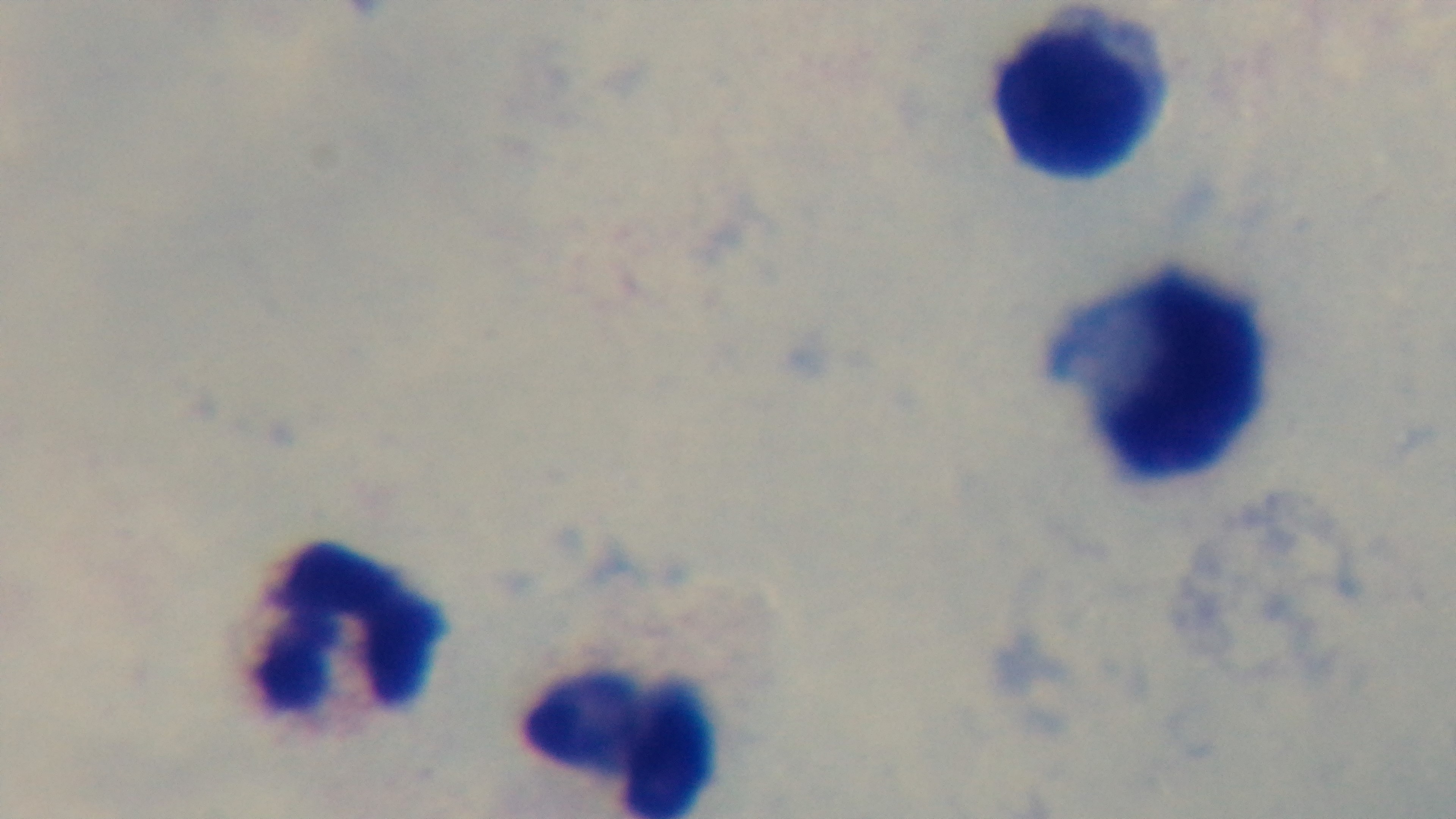

modality: light microscopy
objective: 100x oil immersion
preparation: thick
capture: mounted 4K digital camera
field_of_view: one from the slide
malaria_status: negative
stain: Giemsa